Assess this cell for malaria.
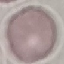
It is uninfected.

Summary:
  - Capture: smartphone camera at the microscope eyepiece
  - Preparation: thin smear
  - Image type: automatically extracted cell patch, resized to 64 × 64 pixels
  - Stain: Giemsa